Name the malaria species.
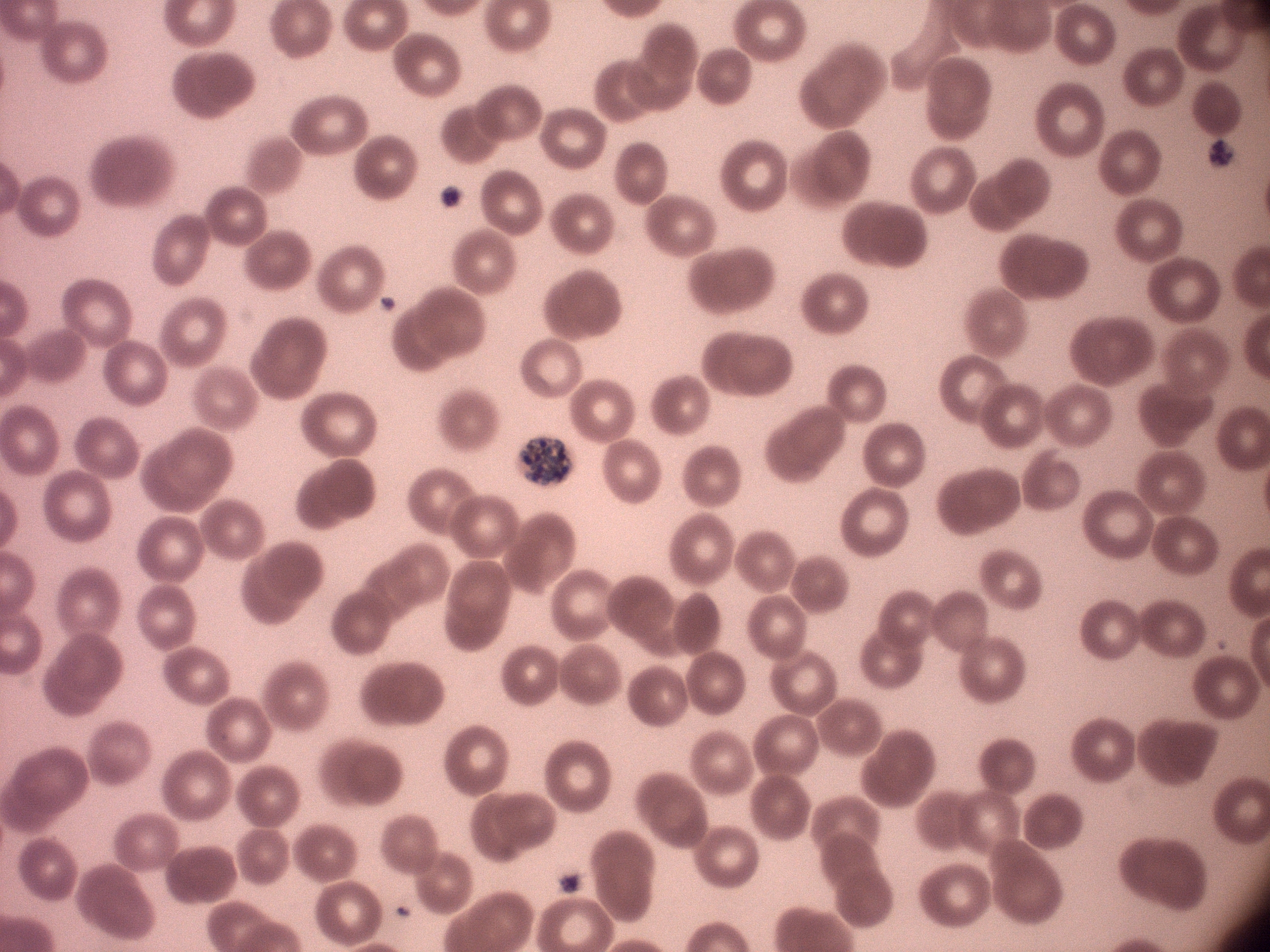
Plasmodium malariae.

Approximate bounding boxes as (x1,y1)-(x2,y2) corner pairs in pixels, from the source annotation, which is not necessarily exhaustive. Schizont locations: (518,435)-(571,487). Giemsa-stained preparation. Image is 1270×952 pixels. Thin blood film. Acquired with a Leica DM2000 optical microscope and its built-in camera. Captured at 100x magnification. Single field of view.